Locate every leukocyte (white blood cell).
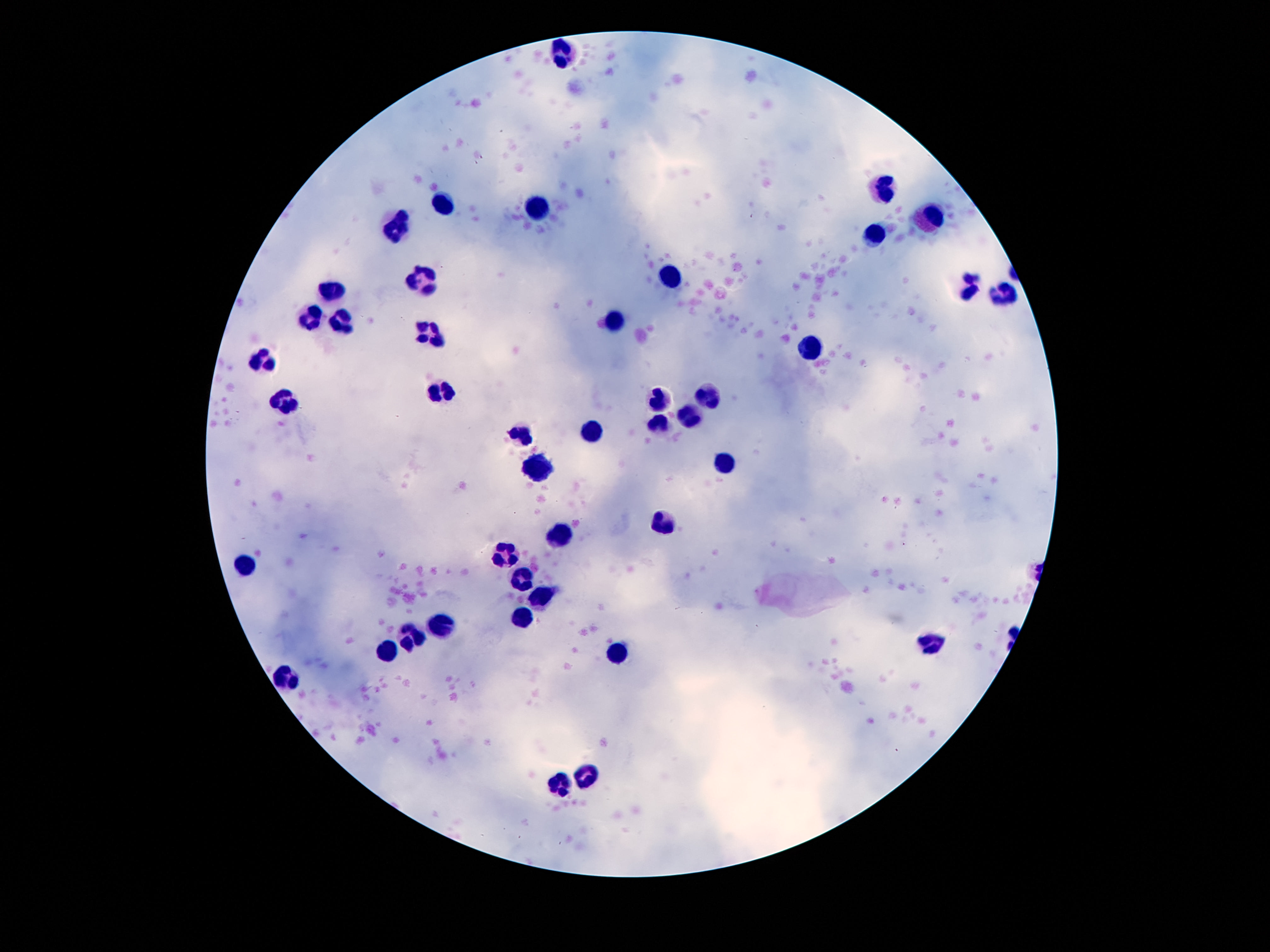
Approximate centers as {x, y} in pixels.
Leukocytes: {565, 54}, {885, 191}, {448, 204}, {540, 208}, {931, 216}, {397, 227}, {877, 236}, {670, 270}, {421, 277}, {969, 285}, {334, 292}, {1003, 292}, {311, 317}, {616, 319}, {343, 323}, {430, 336}, {808, 347}, {262, 361}, {441, 391}, {707, 396}, {285, 400}, {661, 401}, {689, 416}, {658, 420}, {588, 430}, {523, 434}, {723, 464}, {540, 469}, {663, 521}, {560, 534}, {505, 555}, {246, 563}, {523, 580}, {542, 595}, {521, 616}, {441, 625}, {413, 636}, {929, 644}, {390, 653}, {618, 655}, {285, 683}, {584, 775}, {558, 785}.

Summary:
  - Patient malaria status: negative
  - Magnification: 100x
  - Field of view: single
  - Stain: Giemsa
  - Capture: smartphone camera through the microscope eyepiece
  - Image size: 1270×952 pixels
  - Preparation: thick blood film